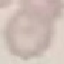
malaria_status: uninfected
preparation: thin blood smear
capture: smartphone through the microscope eyepiece
stain: Giemsa
image_type: cell patch, automatically extracted from a larger field of view and resized to 64 × 64 pixels